Identify the blood parasite species.
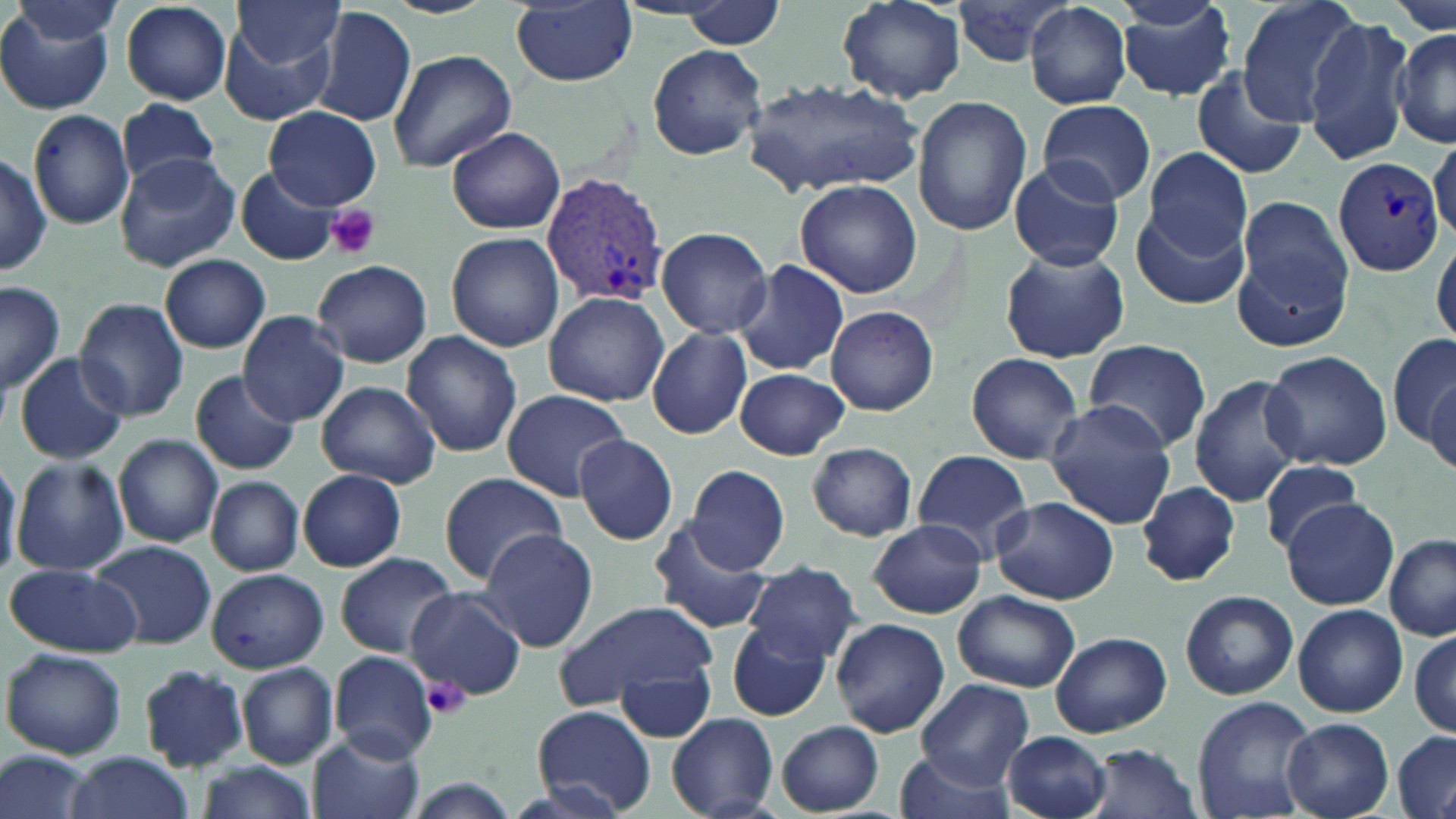

Plasmodium vivax.

Approximate bounding boxes as (x1, y1, x2, y2) in pixels. Platelet locations: (325, 205, 380, 260). Uninfected red blood cell locations: (231, 0, 345, 71), (947, 0, 1074, 71), (1234, 0, 1364, 123), (1392, 0, 1453, 36), (510, 1, 638, 87), (837, 1, 966, 104), (1115, 1, 1237, 100), (120, 2, 232, 104), (679, 2, 786, 50), (1025, 3, 1132, 109), (311, 6, 417, 128), (0, 8, 115, 114), (1302, 16, 1416, 168), (1391, 25, 1456, 149), (220, 26, 335, 123), (647, 44, 768, 160), (388, 50, 516, 172), (1188, 68, 1309, 180), (748, 77, 925, 199), (912, 95, 1032, 236), (117, 97, 220, 189), (1037, 99, 1155, 204), (265, 107, 381, 208), (28, 108, 135, 230), (447, 127, 564, 235), (1429, 134, 1455, 241), (1142, 149, 1252, 258), (0, 153, 51, 276), (114, 153, 242, 271), (1007, 158, 1127, 272), (237, 169, 337, 265), (791, 181, 925, 300), (1235, 193, 1354, 327), (1131, 205, 1249, 311), (658, 225, 774, 340), (1432, 231, 1456, 351), (445, 233, 563, 352), (997, 246, 1131, 363), (161, 255, 271, 353), (312, 259, 432, 367), (733, 259, 848, 376), (0, 279, 65, 399), (543, 291, 669, 406), (74, 297, 190, 422), (825, 306, 939, 416), (237, 310, 352, 426), (646, 324, 751, 441), (1387, 329, 1456, 457), (401, 330, 523, 459), (1080, 341, 1215, 451), (1262, 350, 1391, 468), (965, 353, 1083, 464), (11, 354, 128, 466), (735, 368, 850, 460), (190, 369, 301, 475), (1424, 373, 1455, 470), (1189, 374, 1309, 506), (316, 381, 441, 489), (500, 391, 630, 500), (1041, 403, 1177, 529), (114, 434, 224, 546), (572, 434, 680, 545), (807, 442, 919, 540), (914, 450, 1031, 555), (0, 451, 21, 576), (10, 459, 130, 574), (1259, 459, 1365, 554), (685, 465, 790, 575), (297, 469, 407, 571), (436, 473, 568, 584), (206, 476, 304, 576), (1134, 480, 1240, 585), (988, 494, 1120, 604), (1282, 498, 1399, 610), (646, 518, 772, 636), (866, 520, 987, 619), (477, 528, 598, 651), (1385, 534, 1456, 641), (89, 539, 217, 648), (333, 550, 460, 659), (744, 559, 862, 665), (6, 563, 144, 659), (206, 568, 329, 673), (406, 588, 527, 702), (953, 589, 1082, 691), (1180, 589, 1298, 699), (552, 597, 718, 716), (1293, 604, 1408, 717), (830, 617, 950, 738), (724, 620, 832, 721), (1409, 625, 1456, 736), (1051, 632, 1171, 737), (3, 648, 126, 758), (329, 651, 439, 763), (238, 663, 337, 767), (615, 663, 717, 746), (136, 664, 250, 771), (915, 678, 1032, 787), (1191, 696, 1317, 819), (530, 703, 659, 818), (666, 712, 777, 818), (1282, 717, 1392, 817), (776, 720, 885, 815), (1000, 729, 1113, 819), (309, 730, 424, 819), (1390, 731, 1456, 819), (1080, 742, 1203, 818), (0, 748, 95, 819), (895, 750, 1018, 819), (64, 753, 195, 819), (195, 761, 319, 819), (400, 779, 521, 817). Plasmodium vivax-infected red blood cell locations: (1334, 156, 1446, 277), (539, 170, 672, 308). Thin blood smear. May-Grünwald-Giemsa stain. Light microscopy. One field of a larger specimen. 1000x magnification. Image is 1456×819 pixels.